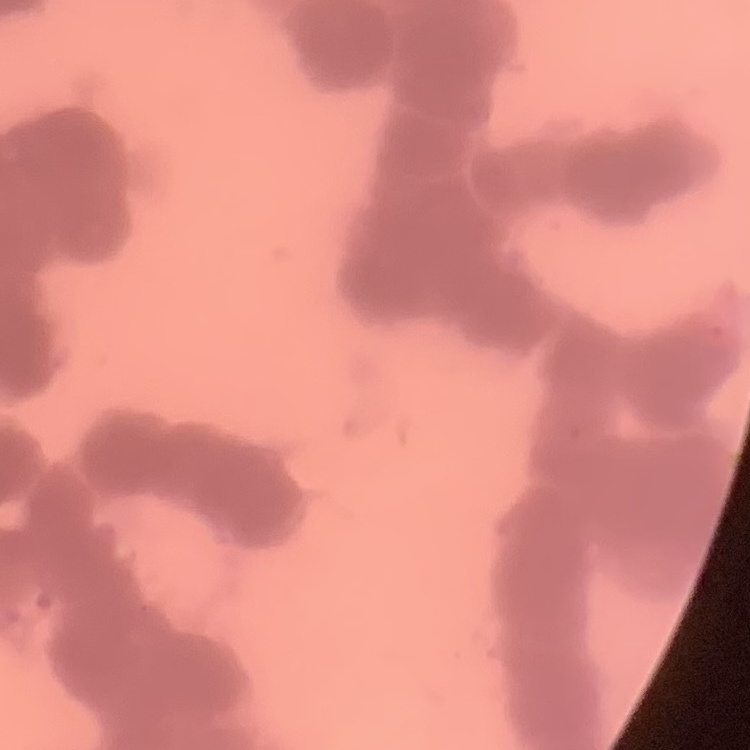

Summary:
  - Erythrocyte morphology: rouleaux formation
  - Image type: square crop of a larger photomicrograph
  - Stain: Field's or Giemsa
  - Preparation: thin blood film